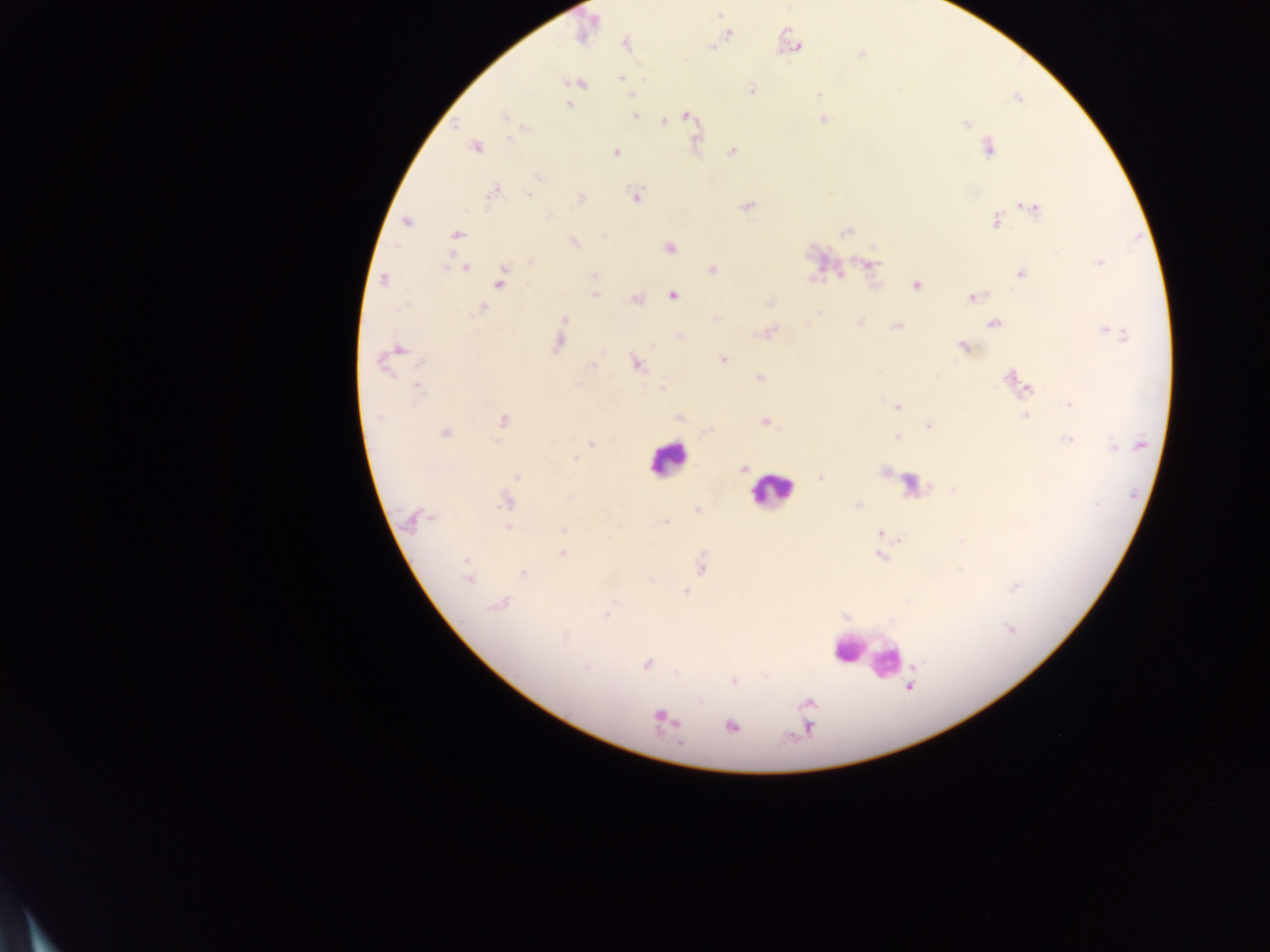 Approximate centers as (x, y) in pixels. Leukocyte locations: (667, 459), (770, 490), (865, 656). Plasmodium parasite locations: (719, 14), (586, 28), (729, 35), (626, 44), (795, 45), (711, 48), (860, 54), (622, 78), (578, 83), (751, 91), (818, 95), (632, 96), (1018, 98), (568, 105), (503, 115), (635, 116), (686, 116), (822, 119), (663, 121), (965, 123), (511, 139), (477, 146), (988, 149), (616, 152), (732, 152), (538, 176), (493, 193), (528, 194), (635, 196), (580, 198), (745, 207), (1031, 208), (548, 216), (407, 222), (995, 222), (846, 231), (456, 234), (574, 243), (669, 247), (531, 262), (1099, 262), (871, 263), (465, 268), (712, 269), (1020, 274), (594, 276), (384, 279), (500, 279), (917, 286), (594, 295), (672, 296), (974, 297), (636, 299), (771, 303), (481, 309), (564, 319), (860, 322), (806, 323), (995, 323), (895, 326), (768, 334), (1119, 334), (557, 343), (963, 347), (399, 349), (723, 358), (383, 363), (422, 363), (636, 365), (592, 366), (760, 378), (1013, 381), (1024, 384), (417, 387), (661, 389), (1069, 405), (898, 406), (1025, 415), (379, 417), (678, 418), (503, 419), (765, 422), (929, 426), (445, 433), (897, 437), (1067, 439), (591, 444), (1114, 446), (575, 459), (743, 468), (517, 476), (821, 477), (569, 498), (506, 501), (857, 506), (697, 510), (412, 519), (664, 522), (508, 527), (564, 530), (880, 532), (562, 554), (880, 556), (702, 568), (523, 573), (467, 578), (1015, 587), (685, 592), (500, 603), (607, 615), (1010, 629), (565, 636), (646, 664), (585, 668), (734, 681), (909, 686), (807, 703), (664, 719), (732, 726), (808, 727). Image is 1270×952 pixels. Sample from Ghana. One field of view. Photographed through a microscope with a mobile-phone camera. Thick blood smear.